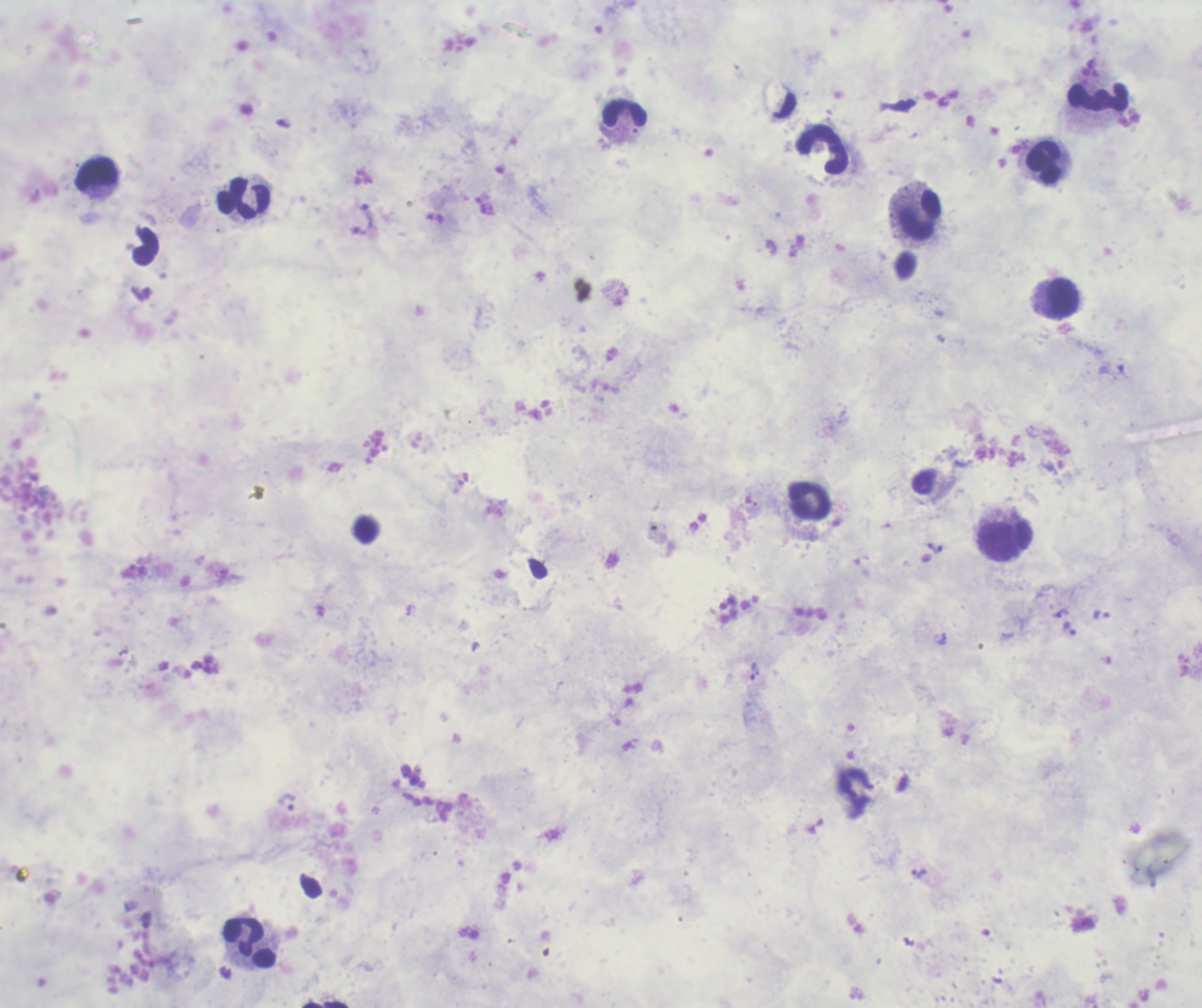
coordinate format = approximate centers as (x, y) in pixels
leukocyte locations = (1096, 97), (625, 113), (823, 150), (1044, 163), (97, 175), (243, 198), (920, 215), (146, 247), (1061, 297), (811, 500), (1007, 541), (250, 943)
trophozoite locations = (368, 215), (935, 548), (1061, 613), (1100, 614), (1070, 630), (753, 671), (287, 802), (919, 873)
field of view = one from this slide
background quality = poor
stain = Romanowsky
magnification = 100x
image size = 1202×1008 pixels
result = malaria parasites identified
context = previously used in an actual diagnosis
preparation = thick smear of blood